Classify this cell by malaria status.
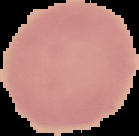
Uninfected.

image size = 139×136 pixels
preparation = thin blood film
image type = segmented cell region with the area outside set to black